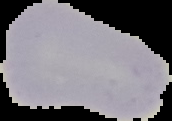
Malaria status: uninfected. Segmented cell region on a black background. Image is 172×121 pixels. From a thin blood film.